Describe the morphology of the red blood cells.
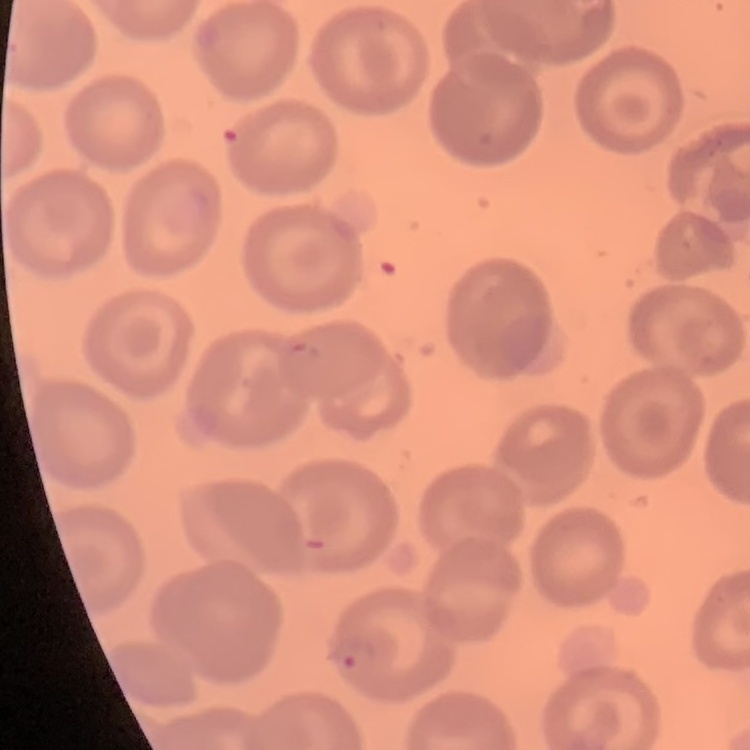
They show no rouleaux formation.

Summary:
  - Image type: one tile cut from a larger photomicrograph
  - Preparation: thin blood smear
  - Stain: Field's or Giemsa